Point out every Plasmodium parasite.
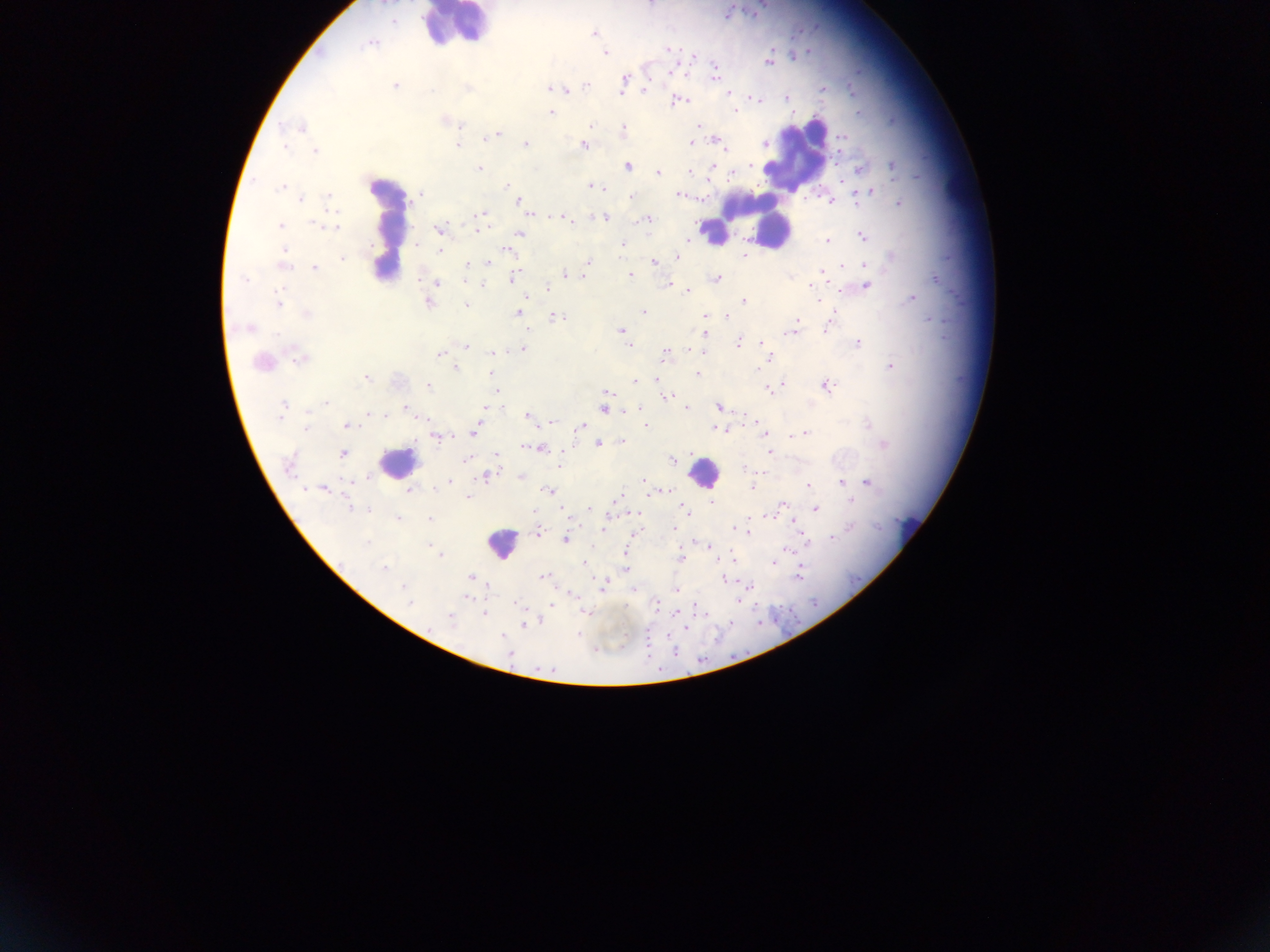

Approximate centers as [x, y] in pixels.
Plasmodium parasites: [394, 22], [594, 33], [371, 43], [668, 49], [605, 54], [693, 57], [769, 61], [671, 72], [714, 76], [624, 82], [586, 85], [395, 86], [468, 87], [551, 87], [566, 89], [823, 89], [645, 90], [728, 93], [787, 97], [754, 98], [677, 101], [736, 111], [551, 113], [459, 125], [698, 125], [591, 126], [303, 128], [624, 131], [493, 135], [842, 138], [718, 141], [691, 143], [525, 144], [457, 145], [583, 145], [285, 146], [725, 149], [315, 150], [627, 166], [712, 167], [893, 167], [479, 168], [859, 169], [735, 171], [690, 172], [658, 173], [507, 186], [591, 186], [281, 188], [598, 188], [868, 192], [420, 195], [679, 195], [328, 196], [630, 197], [301, 199], [858, 199], [831, 200], [519, 201], [900, 203], [479, 215], [556, 216], [604, 217], [566, 219], [648, 219], [318, 224], [280, 225], [333, 227], [439, 229], [478, 230], [519, 233], [862, 237], [688, 240], [826, 240], [622, 245], [506, 249], [440, 251], [284, 253], [744, 255], [890, 256], [677, 257], [342, 259], [283, 262], [489, 262], [589, 262], [468, 263], [654, 263], [865, 266], [314, 268], [588, 268], [821, 271], [566, 275], [583, 275], [630, 276], [514, 278], [935, 278], [245, 279], [716, 279], [436, 283], [669, 284], [482, 285], [866, 286], [811, 287], [547, 288], [688, 291], [912, 299], [279, 301], [744, 301], [428, 302], [467, 305], [644, 311], [517, 313], [307, 315], [727, 316], [705, 317], [556, 318], [797, 320], [795, 325], [827, 326], [249, 327], [620, 331], [789, 332], [705, 334], [738, 342], [762, 343], [858, 343], [630, 346], [466, 347], [523, 350], [694, 350], [493, 352], [699, 352], [665, 353], [440, 354], [300, 356], [769, 358], [261, 362], [890, 367], [457, 368], [491, 373], [697, 374], [366, 378], [656, 378], [635, 381], [782, 384], [428, 386], [778, 386], [826, 386], [495, 390], [770, 391], [608, 392], [665, 397], [326, 403], [282, 406], [719, 406], [484, 407], [686, 408], [406, 409], [604, 409], [370, 413], [383, 415], [527, 416], [756, 421], [867, 424], [646, 425], [758, 425], [346, 426], [580, 427], [306, 428], [717, 429], [762, 430], [474, 432], [804, 433], [437, 436], [793, 436], [622, 441], [598, 443], [884, 444], [532, 447], [539, 448], [769, 452], [343, 453], [465, 460], [672, 460], [289, 465], [558, 466], [367, 476], [485, 476], [521, 477], [643, 481], [449, 482], [867, 482], [840, 483], [809, 485], [752, 488], [323, 489], [410, 491], [548, 491], [467, 497], [616, 499], [851, 501], [711, 502], [783, 503], [350, 508], [590, 508], [815, 509], [367, 510], [685, 510], [637, 514], [770, 515], [397, 518], [430, 519], [849, 526], [673, 528], [603, 529], [734, 529], [748, 532], [538, 533], [832, 538], [565, 540], [366, 543], [432, 545], [709, 547], [785, 549], [626, 552], [439, 554], [681, 558], [732, 559], [772, 562], [583, 563], [382, 569], [625, 569], [799, 572], [542, 576], [471, 577], [723, 580], [603, 584], [404, 588], [676, 589], [409, 602], [655, 603], [551, 605], [586, 613], [485, 614], [675, 614], [450, 618], [524, 625], [685, 627], [503, 636], [510, 653].

{
  "capture": "mobile-phone photograph through a microscope",
  "image_size": "1270×952 pixels",
  "field_of_view": "single",
  "country": "Ghana",
  "leukocyte_locations": "approximate centers as [x, y] in pixels: [453, 25], [794, 155], [759, 219], [384, 225], [713, 233], [397, 462], [703, 472], [910, 530], [501, 543]",
  "preparation": "thick blood film"
}